Identify the parasite.
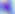

Toxoplasma gondii.

modality = micrograph
magnification = 400x